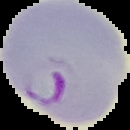

Summary:
  - Malaria status: parasitized
  - Preparation: thin blood film
  - Image size: 130×130 pixels
  - Image type: cell region segmented out of the field of view; surrounding area masked to black